Identify the parasite.
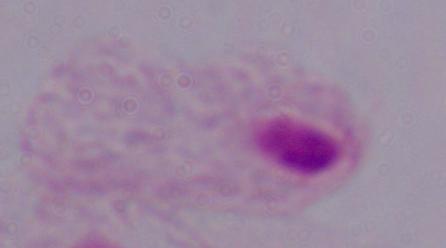

This is a trichomonad.

Summary:
  - Modality: micrograph
  - Magnification: 1000x